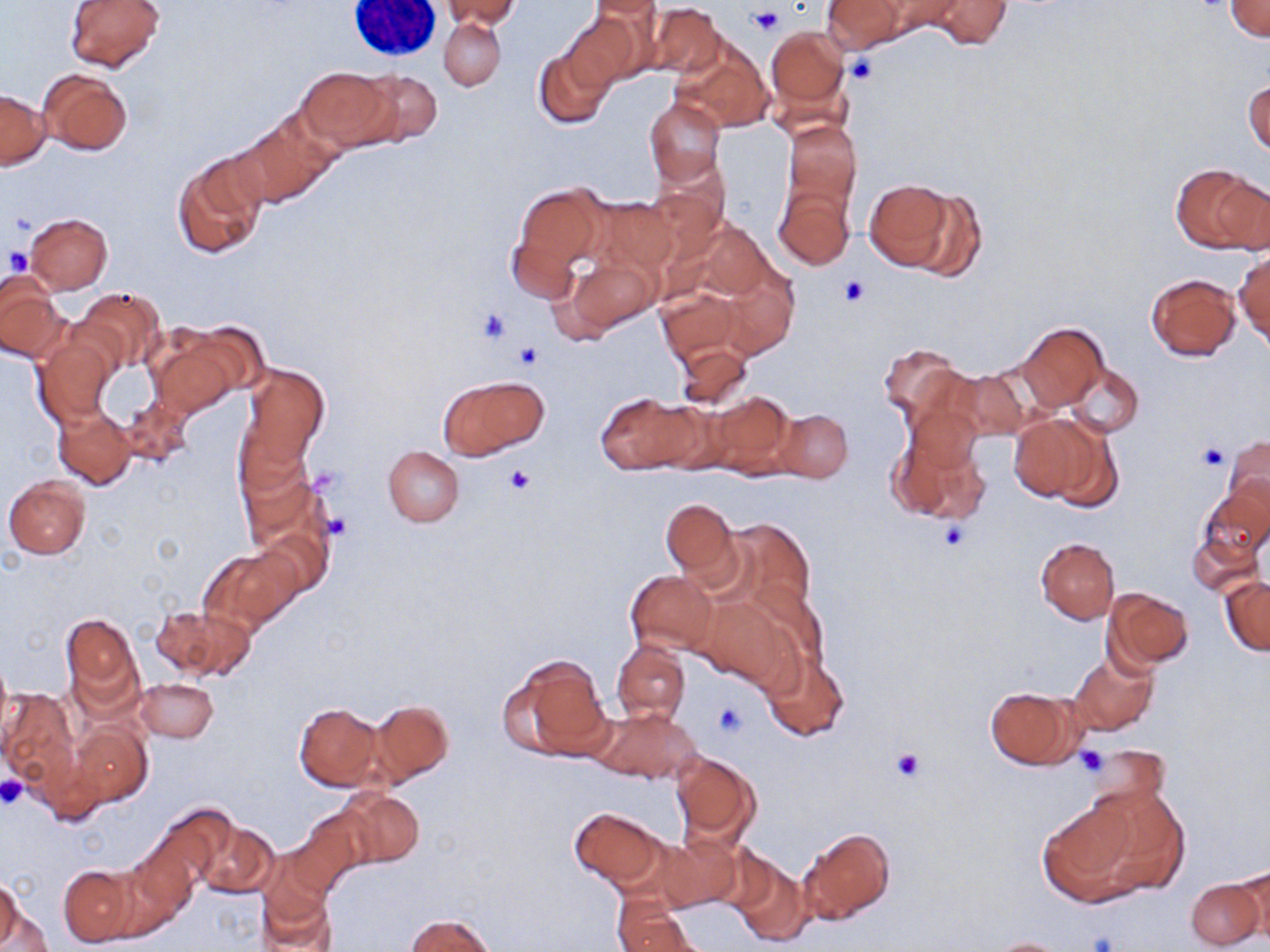
Approximate bounding boxes as named x1/y1/x2/y2 corners in pixels. Uninfected red blood cell locations: (x1=65, y1=0, x2=167, y2=72), (x1=440, y1=0, x2=519, y2=31), (x1=822, y1=0, x2=906, y2=52), (x1=924, y1=0, x2=1013, y2=51), (x1=588, y1=1, x2=664, y2=22), (x1=1225, y1=1, x2=1269, y2=40), (x1=646, y1=2, x2=724, y2=80), (x1=562, y1=13, x2=639, y2=89), (x1=440, y1=17, x2=505, y2=90), (x1=765, y1=26, x2=851, y2=126), (x1=673, y1=36, x2=772, y2=134), (x1=534, y1=47, x2=613, y2=129), (x1=297, y1=66, x2=396, y2=150), (x1=37, y1=68, x2=132, y2=157), (x1=358, y1=71, x2=445, y2=147), (x1=1245, y1=76, x2=1270, y2=160), (x1=1, y1=90, x2=48, y2=169), (x1=644, y1=97, x2=725, y2=185), (x1=234, y1=114, x2=336, y2=207), (x1=782, y1=121, x2=862, y2=209), (x1=173, y1=154, x2=267, y2=259), (x1=1173, y1=163, x2=1267, y2=254), (x1=863, y1=177, x2=960, y2=270), (x1=512, y1=183, x2=607, y2=276), (x1=774, y1=185, x2=855, y2=270), (x1=901, y1=188, x2=987, y2=283), (x1=588, y1=195, x2=680, y2=277), (x1=25, y1=212, x2=112, y2=293), (x1=679, y1=216, x2=779, y2=310), (x1=505, y1=231, x2=582, y2=307), (x1=1234, y1=247, x2=1270, y2=349), (x1=563, y1=255, x2=659, y2=335), (x1=1146, y1=273, x2=1242, y2=361), (x1=0, y1=280, x2=70, y2=364), (x1=657, y1=286, x2=743, y2=365), (x1=74, y1=287, x2=165, y2=376), (x1=1016, y1=321, x2=1106, y2=413), (x1=151, y1=333, x2=240, y2=417), (x1=35, y1=334, x2=116, y2=426), (x1=675, y1=342, x2=753, y2=414), (x1=878, y1=343, x2=970, y2=429), (x1=1063, y1=363, x2=1143, y2=437), (x1=240, y1=365, x2=328, y2=468), (x1=946, y1=368, x2=1031, y2=443), (x1=438, y1=374, x2=547, y2=460), (x1=706, y1=390, x2=796, y2=476), (x1=597, y1=391, x2=702, y2=474), (x1=120, y1=396, x2=193, y2=469), (x1=52, y1=408, x2=136, y2=490), (x1=774, y1=409, x2=853, y2=482), (x1=1014, y1=413, x2=1119, y2=509), (x1=888, y1=426, x2=991, y2=525), (x1=1222, y1=434, x2=1270, y2=519), (x1=383, y1=446, x2=464, y2=526), (x1=237, y1=464, x2=327, y2=557), (x1=3, y1=476, x2=89, y2=559), (x1=1197, y1=486, x2=1269, y2=569), (x1=660, y1=499, x2=737, y2=582), (x1=720, y1=519, x2=816, y2=617), (x1=1188, y1=522, x2=1263, y2=598), (x1=252, y1=526, x2=331, y2=604), (x1=1035, y1=537, x2=1120, y2=625), (x1=200, y1=549, x2=296, y2=633), (x1=626, y1=570, x2=718, y2=653), (x1=1220, y1=575, x2=1270, y2=655), (x1=1104, y1=589, x2=1194, y2=670), (x1=696, y1=595, x2=793, y2=688), (x1=153, y1=604, x2=247, y2=680), (x1=61, y1=613, x2=140, y2=705), (x1=613, y1=639, x2=690, y2=725), (x1=761, y1=652, x2=849, y2=742), (x1=1067, y1=652, x2=1158, y2=736), (x1=500, y1=654, x2=613, y2=763), (x1=136, y1=678, x2=218, y2=742), (x1=985, y1=686, x2=1085, y2=770), (x1=1, y1=688, x2=79, y2=789), (x1=368, y1=700, x2=454, y2=786), (x1=294, y1=701, x2=382, y2=791), (x1=592, y1=707, x2=701, y2=785), (x1=70, y1=721, x2=151, y2=806), (x1=1086, y1=743, x2=1169, y2=816), (x1=671, y1=751, x2=761, y2=845), (x1=338, y1=789, x2=425, y2=866), (x1=1050, y1=796, x2=1174, y2=905), (x1=146, y1=804, x2=237, y2=892), (x1=291, y1=806, x2=377, y2=893), (x1=568, y1=807, x2=669, y2=889), (x1=195, y1=819, x2=279, y2=899), (x1=799, y1=828, x2=896, y2=924), (x1=657, y1=833, x2=742, y2=914), (x1=726, y1=853, x2=812, y2=947), (x1=257, y1=864, x2=337, y2=952), (x1=1231, y1=864, x2=1270, y2=945), (x1=58, y1=866, x2=135, y2=946), (x1=1185, y1=876, x2=1264, y2=950), (x1=1, y1=877, x2=24, y2=949), (x1=614, y1=899, x2=698, y2=952), (x1=3, y1=907, x2=52, y2=951), (x1=406, y1=914, x2=495, y2=951), (x1=987, y1=937, x2=1070, y2=951). Platelet locations: (x1=748, y1=6, x2=781, y2=34), (x1=844, y1=54, x2=878, y2=86), (x1=4, y1=248, x2=33, y2=275), (x1=838, y1=275, x2=871, y2=305), (x1=476, y1=308, x2=512, y2=344), (x1=513, y1=342, x2=542, y2=369), (x1=1197, y1=442, x2=1228, y2=470), (x1=505, y1=464, x2=536, y2=493), (x1=322, y1=511, x2=353, y2=541), (x1=937, y1=520, x2=973, y2=553), (x1=713, y1=702, x2=749, y2=739), (x1=1077, y1=745, x2=1106, y2=776), (x1=892, y1=747, x2=924, y2=781), (x1=0, y1=776, x2=28, y2=810), (x1=1086, y1=931, x2=1119, y2=952). Slide-level diagnosis: no evidence of blood parasites. Thin blood smear. Light microscopy. May-Grünwald-Giemsa stain. 1000x magnification. Image is 1270×952 pixels. Single field of view.